State which parasite is depicted.
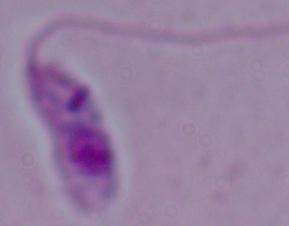
Leishmania.

Photomicrograph. 1000x magnification.